Report the malaria status.
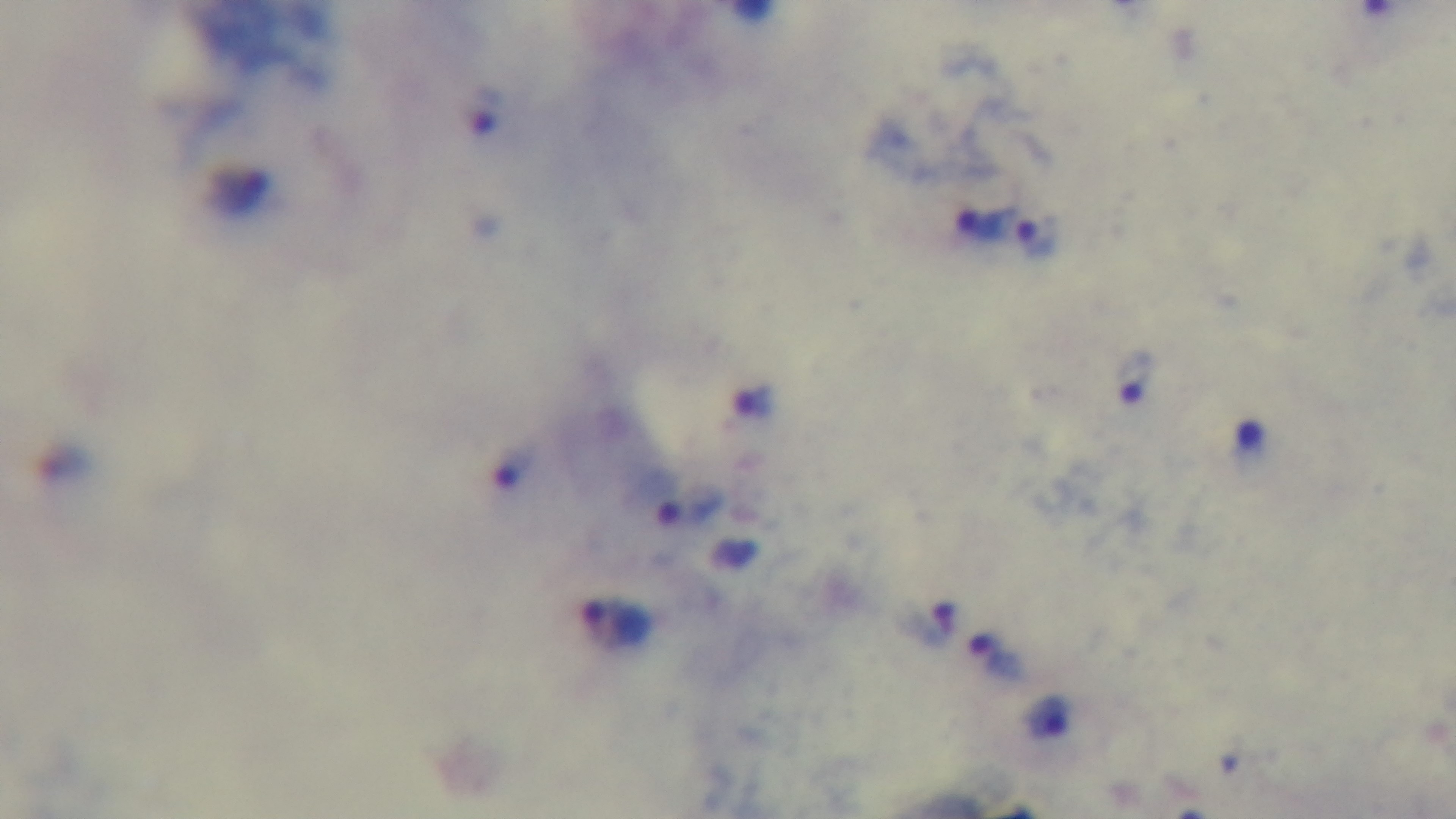
Infected.

modality = light microscopy
objective = 100x oil immersion
stain = Giemsa
capture = mounted 4K digital camera
preparation = thick
field of view = single